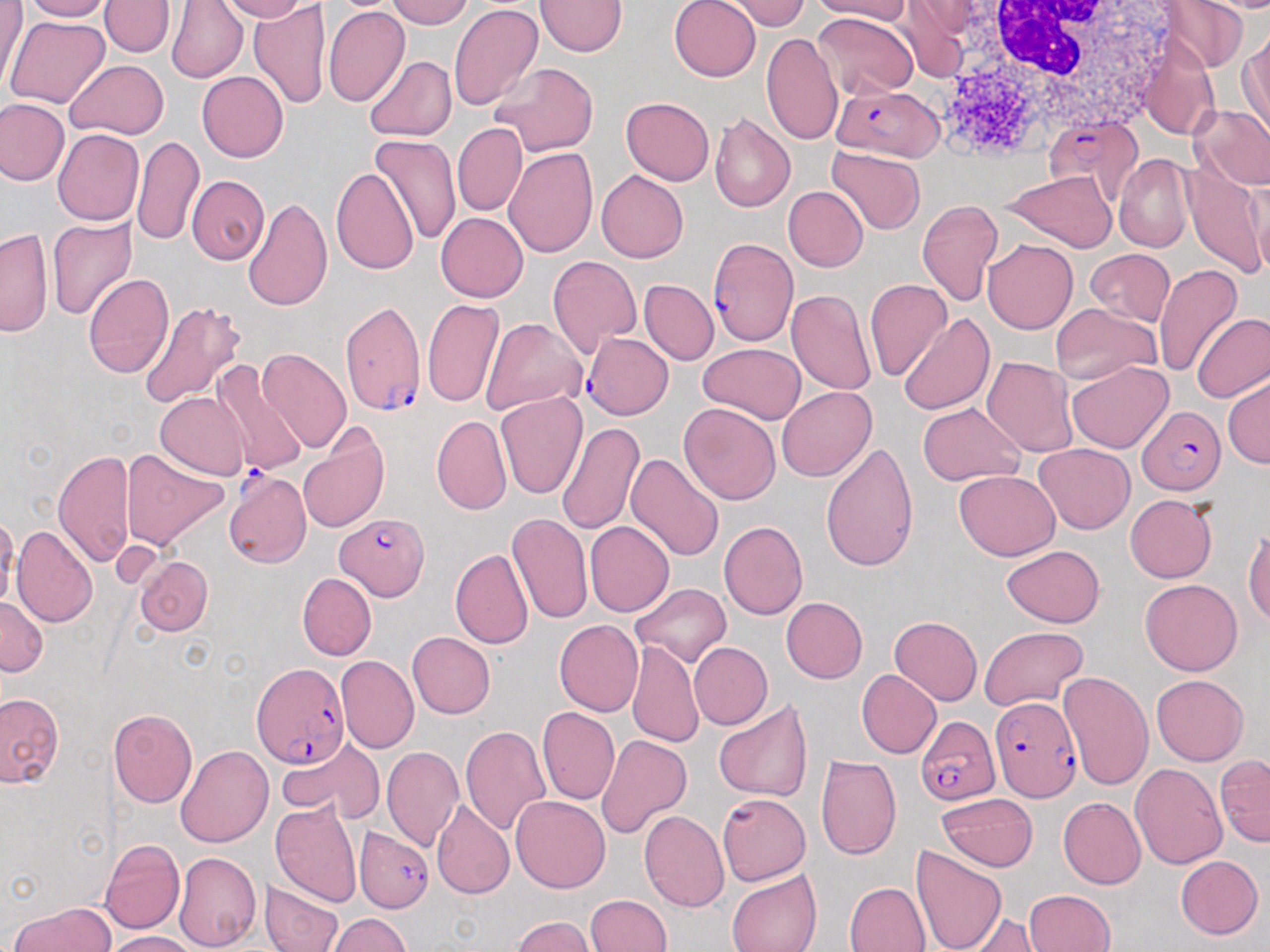

Approximate bounding boxes as [x1, y1, x2, y2] in pixels. White blood cell locations: [937, 0, 1186, 153]. Plasmodium falciparum-infected red blood cell locations: [831, 83, 942, 161], [1042, 114, 1146, 202], [707, 239, 797, 346], [338, 301, 425, 418], [583, 330, 673, 416], [1137, 406, 1226, 496], [223, 471, 310, 569], [334, 511, 430, 601], [253, 661, 350, 767], [989, 693, 1079, 801], [916, 716, 1001, 805], [355, 827, 433, 911]. Uninfected red blood cell locations: [20, 0, 114, 22], [167, 0, 249, 83], [213, 0, 310, 22], [386, 0, 473, 29], [537, 0, 626, 55], [670, 0, 761, 82], [719, 0, 812, 32], [812, 0, 913, 23], [1157, 0, 1250, 75], [0, 1, 28, 92], [100, 1, 175, 57], [449, 2, 544, 111], [249, 3, 332, 110], [894, 4, 970, 82], [325, 6, 410, 107], [812, 11, 918, 101], [4, 14, 110, 108], [1240, 29, 1269, 135], [761, 32, 844, 146], [1139, 43, 1220, 141], [363, 56, 456, 142], [64, 59, 168, 139], [489, 62, 600, 156], [196, 71, 289, 162], [0, 97, 69, 185], [622, 97, 715, 185], [1191, 103, 1270, 191], [709, 112, 795, 215], [452, 122, 526, 216], [53, 129, 144, 226], [370, 133, 462, 246], [133, 134, 204, 245], [827, 146, 925, 235], [503, 148, 598, 256], [1114, 154, 1193, 252], [1182, 156, 1267, 279], [330, 167, 418, 276], [596, 170, 688, 263], [1004, 171, 1116, 252], [186, 175, 269, 264], [783, 185, 868, 272], [243, 197, 332, 313], [916, 200, 1004, 307], [437, 212, 528, 303], [47, 216, 136, 321], [0, 227, 52, 337], [983, 239, 1077, 334], [1085, 248, 1174, 325], [547, 255, 641, 356], [1153, 265, 1242, 377], [83, 273, 175, 379], [639, 279, 718, 366], [864, 279, 952, 382], [787, 288, 878, 396], [423, 298, 504, 408], [138, 301, 246, 410], [1049, 303, 1162, 387], [899, 311, 995, 414], [1192, 312, 1270, 403], [481, 318, 587, 417], [697, 343, 805, 424], [257, 348, 351, 453], [982, 356, 1077, 457], [1066, 360, 1173, 453], [210, 361, 310, 478], [1223, 373, 1269, 469], [777, 387, 876, 481], [155, 392, 251, 480], [494, 393, 586, 499], [916, 402, 1026, 485], [677, 403, 781, 505], [432, 415, 512, 515], [294, 420, 390, 536], [556, 420, 645, 535], [819, 441, 918, 572], [1035, 442, 1134, 534], [122, 447, 228, 550], [55, 451, 135, 567], [626, 452, 725, 563], [953, 469, 1060, 560], [1124, 493, 1218, 582], [506, 512, 592, 625], [585, 521, 674, 617], [718, 521, 808, 620], [11, 525, 98, 628], [1244, 528, 1270, 629], [1001, 545, 1105, 627], [450, 549, 534, 649], [133, 556, 212, 636], [297, 572, 377, 660], [1140, 579, 1243, 676], [628, 583, 730, 669], [0, 596, 47, 676], [781, 596, 868, 683], [887, 617, 982, 706], [555, 620, 644, 717], [979, 625, 1089, 710], [407, 631, 495, 718], [614, 639, 698, 838], [627, 640, 704, 750], [689, 642, 773, 730], [335, 654, 419, 753], [856, 670, 941, 759], [1058, 670, 1153, 792], [1151, 675, 1249, 766], [0, 692, 64, 787], [713, 700, 814, 803], [536, 706, 619, 805], [108, 710, 197, 807], [459, 725, 551, 836], [596, 734, 692, 839], [278, 739, 380, 819], [175, 744, 273, 847], [381, 746, 464, 851], [1215, 753, 1270, 845], [814, 755, 902, 860], [1130, 761, 1228, 869], [718, 792, 810, 884], [936, 792, 1037, 871], [511, 795, 611, 894], [1057, 797, 1146, 890], [271, 799, 363, 907], [430, 799, 514, 899], [639, 809, 730, 911], [101, 839, 184, 935], [910, 843, 1007, 952], [173, 851, 261, 952], [1175, 855, 1263, 939], [725, 869, 821, 952], [259, 878, 346, 952], [844, 882, 931, 952], [1024, 889, 1116, 952], [584, 894, 671, 952], [9, 901, 116, 952], [326, 913, 411, 951], [962, 914, 1045, 952], [512, 916, 600, 952], [103, 930, 200, 951]. Slide-level diagnosis: Plasmodium falciparum. One field of a larger specimen. Image is 1270×952 pixels. May-Grünwald-Giemsa stain. Optical microscopy. Thin blood smear. 1000x magnification.